State the preparation type.
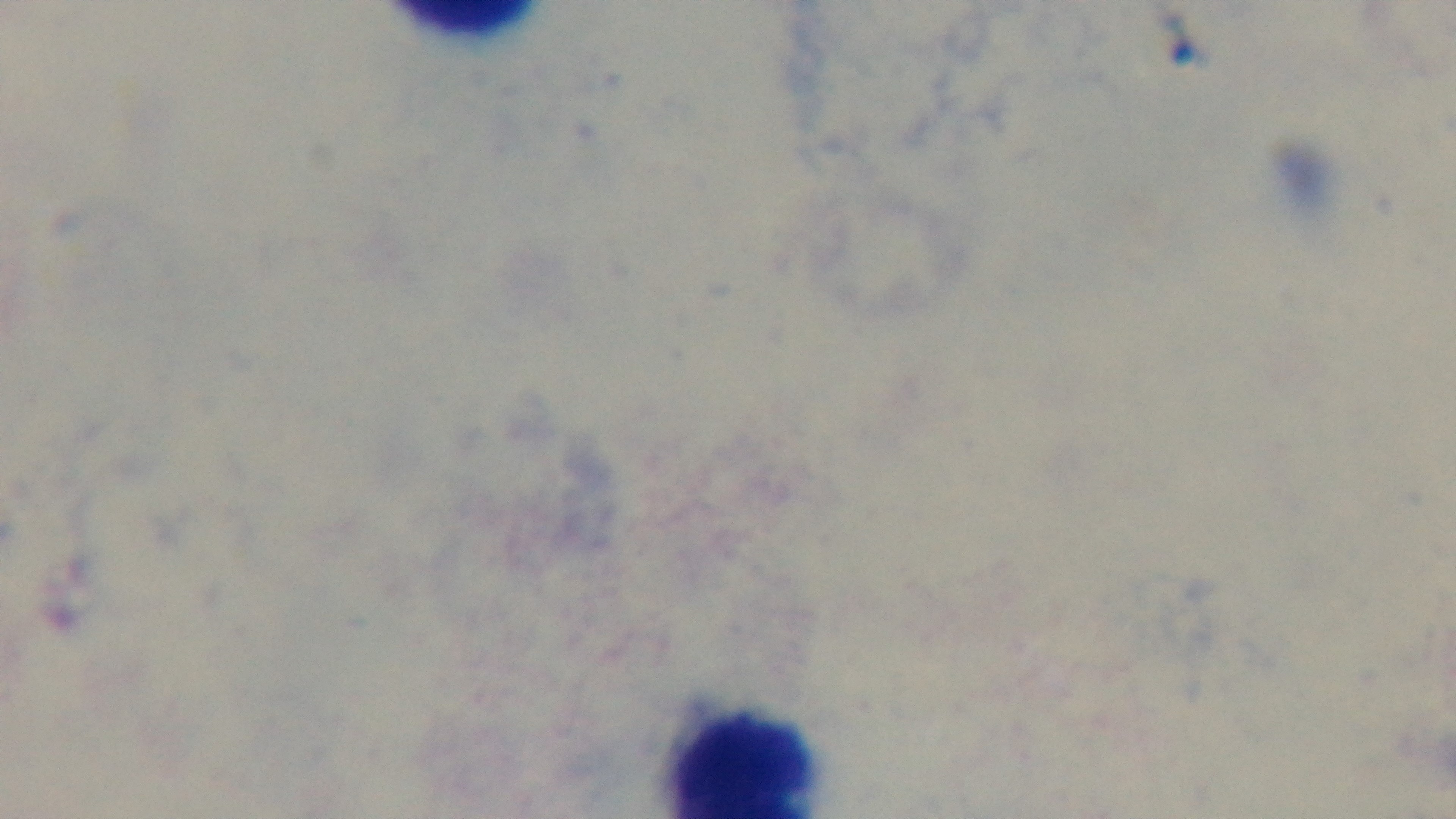

It is a thick blood film.

objective = 100x oil immersion
stain = Giemsa
capture = mounted 4K digital camera
modality = light microscopy
field of view = single
malaria status = uninfected